Assess this cell for malaria.
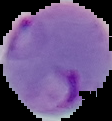
Parasitized.

The area outside the segmented cell region is set to black. Image is 112×121 pixels. From a thin blood film.